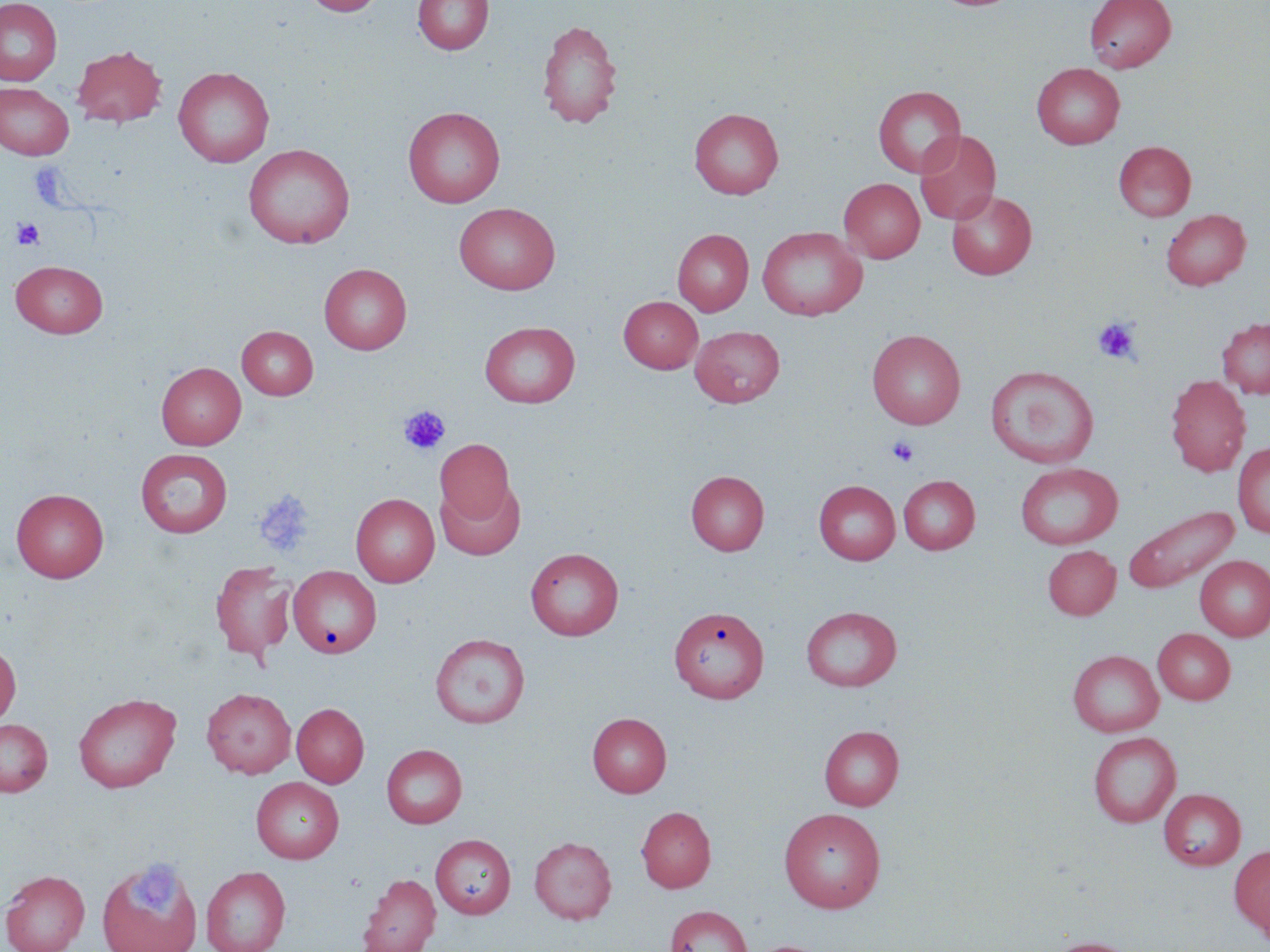
slide-level diagnosis = no evidence of blood parasites
platelet locations = approximate bounding boxes as (x1,y1)-(x2,y2) corner pairs in pixels: (11,218)-(44,250), (1093,316)-(1142,365), (399,405)-(450,455), (887,436)-(920,467), (254,489)-(315,558), (125,861)-(185,921)
magnification = 1000x
uninfected red blood cell locations = approximate bounding boxes as (x1,y1)-(x2,y2) corner pairs in pixels: (0,0)-(62,86), (303,0)-(385,16), (413,0)-(493,55), (1084,0)-(1176,72), (536,19)-(622,129), (72,45)-(166,127), (1031,63)-(1125,149), (173,66)-(274,167), (0,82)-(74,160), (873,85)-(965,177), (403,106)-(505,208), (689,108)-(783,199), (914,130)-(1001,225), (1114,141)-(1196,221), (243,144)-(355,248), (839,178)-(925,263), (946,189)-(1037,280), (454,202)-(560,295), (1160,208)-(1251,290), (757,226)-(867,321), (672,229)-(753,316), (11,260)-(107,337), (319,263)-(412,354), (618,296)-(703,373), (1217,317)-(1270,399), (480,321)-(580,407), (689,324)-(784,408), (237,326)-(318,399), (867,329)-(966,429), (156,362)-(246,449), (986,364)-(1099,468), (1165,374)-(1250,476), (435,438)-(515,526), (1233,443)-(1270,538), (136,449)-(233,537), (1015,463)-(1122,549), (685,470)-(769,556), (898,475)-(980,554), (814,480)-(900,564), (436,481)-(525,560), (11,488)-(109,582), (350,493)-(439,587), (1123,504)-(1238,594), (1042,545)-(1121,619), (525,547)-(624,640), (1195,555)-(1270,640), (210,560)-(296,662), (288,566)-(381,658), (670,605)-(768,703), (801,606)-(902,691), (1153,628)-(1235,704), (430,633)-(530,728), (0,642)-(20,727), (1067,650)-(1164,736), (201,687)-(296,778), (73,692)-(182,793), (292,703)-(369,787), (587,713)-(672,797), (0,718)-(52,796), (819,725)-(904,810), (1087,731)-(1181,828), (381,744)-(467,828), (251,776)-(344,863), (1158,788)-(1246,870), (636,806)-(716,892), (779,807)-(886,912), (430,834)-(515,918), (529,836)-(617,924), (1230,845)-(1270,939), (97,856)-(203,952), (200,866)-(291,952), (1,869)-(90,952), (358,873)-(441,952), (664,905)-(752,952), (1042,936)-(1144,952)
stain = May-Grünwald-Giemsa
modality = light microscopy
image size = 1270×952 pixels
preparation = thin blood film
field of view = one of a larger specimen